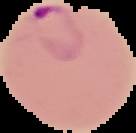
Malaria status: parasitized. The area outside the segmented cell region is set to black. Image is 136×133 pixels. From a thin blood smear.